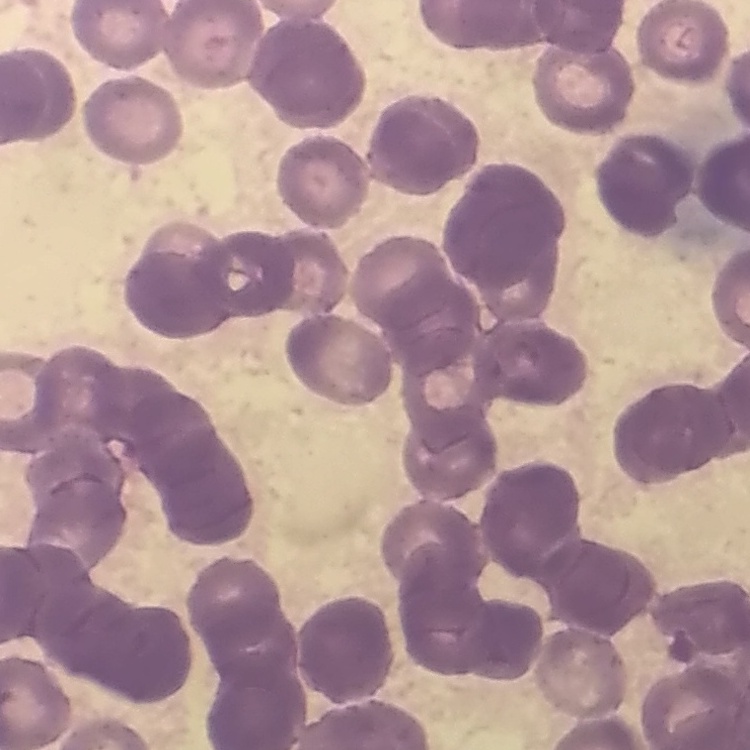

Summary:
  - Red blood cell morphology: rouleaux formation
  - Preparation: thin blood smear
  - Stain: Field's or Giemsa
  - Image type: square crop of a larger photomicrograph